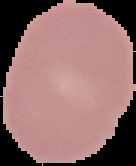
Image is 136×166 pixels. From a thin blood smear. Malaria status: uninfected. Segmented cell region on a black background.